Assess this cell for malaria.
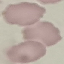

Uninfected.

Summary:
  - Preparation: thin blood film
  - Capture: smartphone camera at the microscope eyepiece
  - Image type: automatically extracted cell patch, resized to 64 × 64 pixels
  - Stain: Giemsa